Identify the blood parasite species.
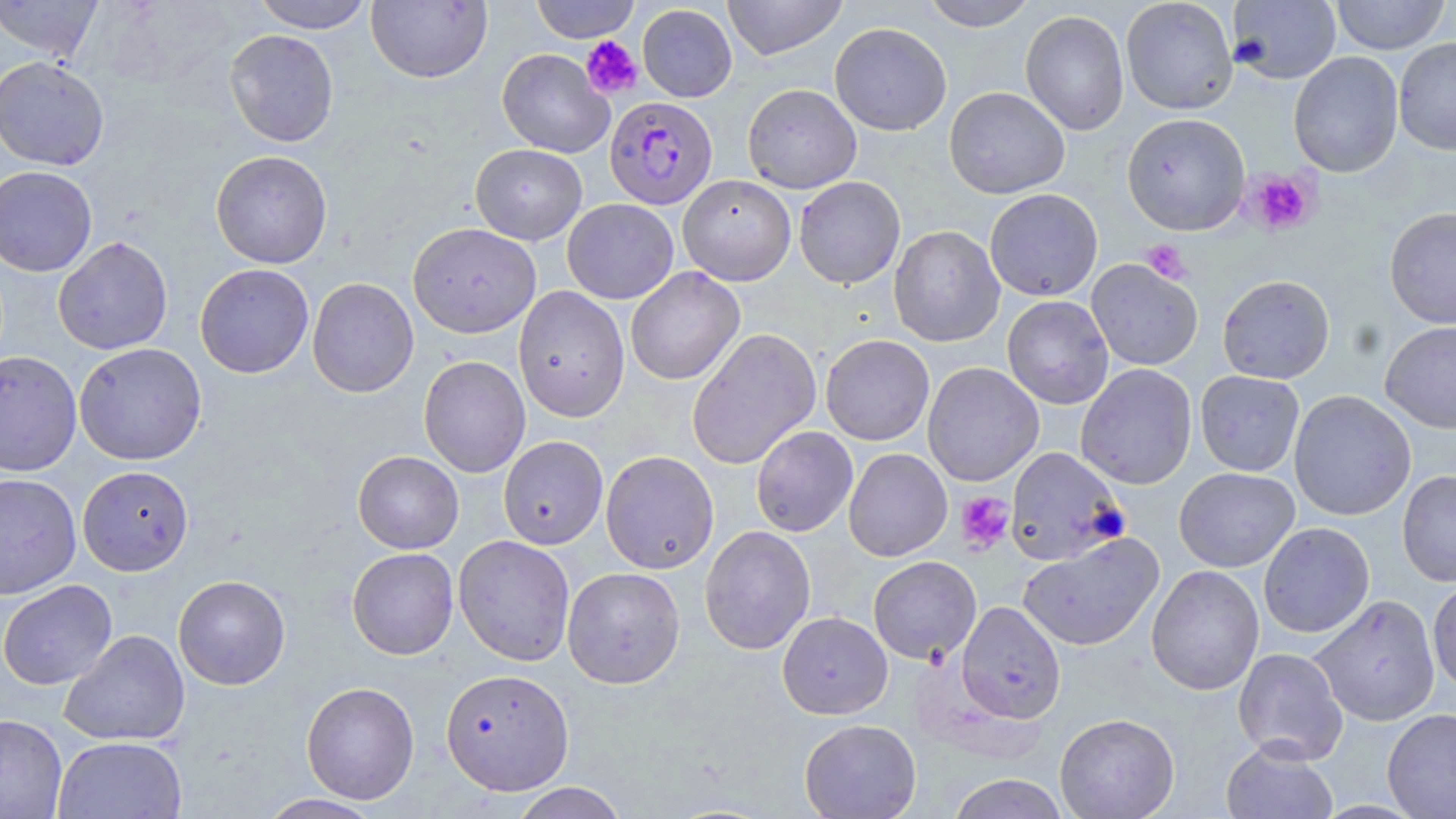
Plasmodium falciparum.

field of view = one of a larger specimen
preparation = thin blood smear
uninfected red blood cell locations = approximate bounding boxes as named x1/y1/x2/y2 corners in pixels: (x1=0, y1=0, x2=104, y2=61), (x1=250, y1=0, x2=375, y2=33), (x1=530, y1=0, x2=640, y2=43), (x1=722, y1=0, x2=848, y2=60), (x1=920, y1=0, x2=1039, y2=31), (x1=1121, y1=0, x2=1238, y2=115), (x1=1228, y1=0, x2=1341, y2=84), (x1=1331, y1=0, x2=1451, y2=54), (x1=366, y1=1, x2=492, y2=84), (x1=637, y1=4, x2=737, y2=102), (x1=1020, y1=10, x2=1130, y2=136), (x1=829, y1=22, x2=952, y2=136), (x1=224, y1=29, x2=339, y2=147), (x1=1394, y1=36, x2=1456, y2=155), (x1=497, y1=48, x2=614, y2=157), (x1=1288, y1=51, x2=1404, y2=178), (x1=0, y1=55, x2=110, y2=171), (x1=742, y1=83, x2=862, y2=194), (x1=944, y1=86, x2=1070, y2=199), (x1=1122, y1=113, x2=1250, y2=235), (x1=470, y1=144, x2=587, y2=245), (x1=210, y1=150, x2=333, y2=268), (x1=0, y1=166, x2=97, y2=276), (x1=678, y1=174, x2=796, y2=285), (x1=794, y1=176, x2=905, y2=289), (x1=984, y1=188, x2=1103, y2=301), (x1=562, y1=198, x2=679, y2=304), (x1=1385, y1=207, x2=1456, y2=328), (x1=407, y1=222, x2=541, y2=339), (x1=888, y1=225, x2=1005, y2=347), (x1=53, y1=236, x2=173, y2=355), (x1=1086, y1=258, x2=1203, y2=371), (x1=194, y1=263, x2=314, y2=378), (x1=625, y1=267, x2=745, y2=385), (x1=1217, y1=274, x2=1335, y2=384), (x1=307, y1=277, x2=419, y2=398), (x1=513, y1=286, x2=630, y2=423), (x1=1002, y1=296, x2=1114, y2=409), (x1=1380, y1=321, x2=1456, y2=433), (x1=686, y1=327, x2=822, y2=470), (x1=820, y1=334, x2=934, y2=445), (x1=74, y1=343, x2=207, y2=465), (x1=0, y1=350, x2=82, y2=476), (x1=419, y1=355, x2=531, y2=478), (x1=922, y1=362, x2=1044, y2=486), (x1=1076, y1=363, x2=1198, y2=490), (x1=1195, y1=371, x2=1305, y2=476), (x1=1289, y1=390, x2=1416, y2=521), (x1=751, y1=426, x2=858, y2=537), (x1=498, y1=435, x2=608, y2=549), (x1=1005, y1=447, x2=1127, y2=566), (x1=843, y1=448, x2=952, y2=561), (x1=352, y1=450, x2=464, y2=553), (x1=600, y1=450, x2=719, y2=573), (x1=78, y1=465, x2=193, y2=575), (x1=1174, y1=467, x2=1299, y2=572), (x1=1397, y1=469, x2=1456, y2=586), (x1=0, y1=473, x2=82, y2=599), (x1=1258, y1=522, x2=1375, y2=638), (x1=699, y1=525, x2=816, y2=655), (x1=1018, y1=532, x2=1164, y2=652), (x1=453, y1=535, x2=576, y2=666), (x1=347, y1=547, x2=458, y2=659), (x1=868, y1=556, x2=981, y2=664), (x1=1146, y1=565, x2=1264, y2=696), (x1=562, y1=566, x2=685, y2=688), (x1=173, y1=575, x2=290, y2=690), (x1=1428, y1=578, x2=1456, y2=695), (x1=0, y1=579, x2=117, y2=690), (x1=1310, y1=595, x2=1441, y2=727), (x1=957, y1=601, x2=1066, y2=723), (x1=777, y1=612, x2=892, y2=719), (x1=60, y1=629, x2=190, y2=746), (x1=1233, y1=648, x2=1348, y2=765), (x1=441, y1=668, x2=574, y2=795), (x1=301, y1=682, x2=420, y2=804), (x1=1382, y1=708, x2=1456, y2=819), (x1=1055, y1=713, x2=1180, y2=818), (x1=0, y1=714, x2=67, y2=818), (x1=799, y1=718, x2=922, y2=819), (x1=53, y1=736, x2=188, y2=819), (x1=1221, y1=741, x2=1338, y2=819), (x1=946, y1=774, x2=1070, y2=819), (x1=508, y1=782, x2=629, y2=818), (x1=254, y1=793, x2=387, y2=818)
image size = 1456×819 pixels
modality = optical microscopy
magnification = 1000x
Plasmodium falciparum-infected red blood cell locations = approximate bounding boxes as named x1/y1/x2/y2 corners in pixels: (x1=605, y1=96, x2=717, y2=209)
stain = May-Grünwald-Giemsa
platelet locations = approximate bounding boxes as named x1/y1/x2/y2 corners in pixels: (x1=580, y1=35, x2=643, y2=98), (x1=1246, y1=169, x2=1319, y2=235), (x1=1141, y1=240, x2=1191, y2=285), (x1=955, y1=492, x2=1014, y2=553)